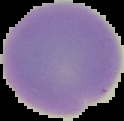 Malaria status: uninfected. Image is 124×121 pixels. Cell region segmented out of the field of view; the surrounding area is masked to black. From a thin blood smear.